Identify the blood parasite species.
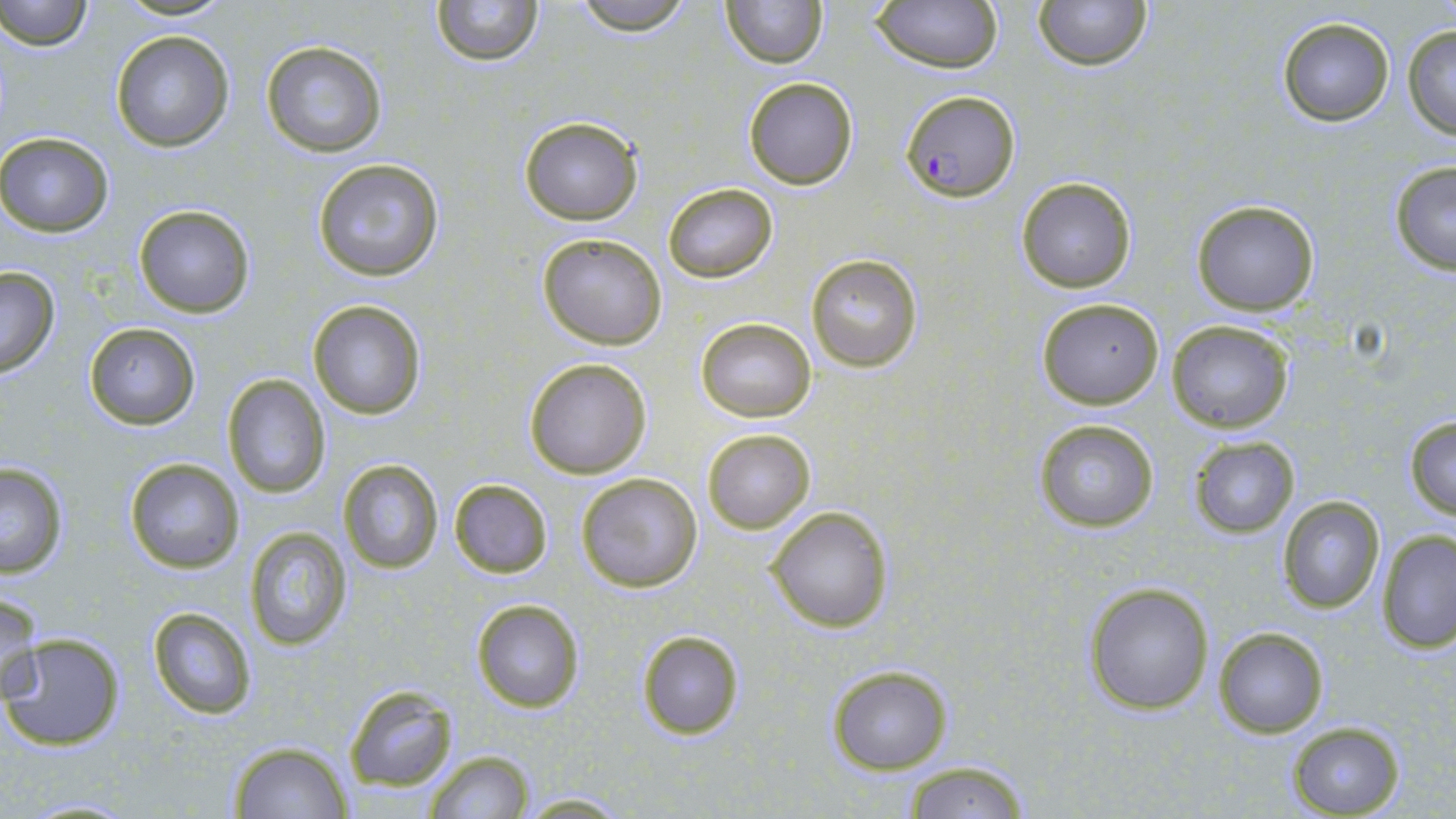

Plasmodium falciparum.

Approximate bounding boxes as (x1, y1, x2, y2) in pixels. Plasmodium falciparum-infected red blood cell locations: (900, 91, 1019, 202). Uninfected red blood cell locations: (1, 0, 95, 53), (430, 0, 546, 66), (568, 0, 698, 34), (720, 0, 827, 69), (1034, 0, 1151, 71), (871, 1, 1004, 74), (1275, 16, 1397, 127), (1401, 23, 1456, 140), (110, 30, 234, 152), (259, 39, 387, 157), (741, 76, 859, 190), (518, 115, 644, 225), (0, 132, 114, 237), (311, 158, 446, 282), (1388, 161, 1456, 275), (1016, 176, 1137, 294), (662, 182, 778, 284), (1191, 200, 1321, 316), (133, 205, 255, 317), (537, 234, 667, 350), (805, 254, 922, 372), (0, 266, 61, 378), (1034, 297, 1165, 408), (308, 299, 427, 421), (696, 317, 816, 422), (1166, 320, 1295, 434), (84, 322, 200, 429), (523, 356, 653, 479), (222, 374, 332, 499), (1404, 415, 1456, 519), (1032, 418, 1160, 533), (702, 427, 816, 534), (1186, 435, 1301, 537), (124, 457, 244, 574), (336, 458, 445, 574), (0, 462, 70, 578), (575, 471, 703, 593), (447, 477, 554, 579), (1276, 495, 1386, 613), (765, 505, 893, 634), (243, 527, 352, 650), (1375, 529, 1456, 655), (1083, 581, 1215, 715), (1, 590, 44, 707), (472, 600, 585, 713), (147, 607, 258, 718), (1212, 626, 1329, 738), (635, 629, 744, 741), (2, 632, 126, 751), (827, 665, 953, 774), (343, 686, 460, 793), (1284, 720, 1406, 819), (227, 742, 354, 819), (426, 749, 533, 819), (900, 760, 1030, 818), (514, 792, 635, 816). Single field of view. Image is 1456×819 pixels. Captured at 1000x magnification. May-Grünwald-Giemsa-stained preparation. Optical microscopy. Thin blood smear.